Identify the parasite.
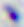
This is Toxoplasma gondii.

Captured at 400x magnification. Photomicrograph.